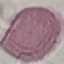

Malaria status: uninfected. Cell patch, automatically extracted from a larger field of view and resized to 64 × 64 pixels. Thin blood film. Giemsa-stained preparation. Acquired by smartphone through the microscope eyepiece.